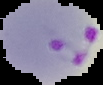 Image is 103×85 pixels. Result: Plasmodium parasites detected. The area outside the segmented cell region is set to black. From a thin blood smear.